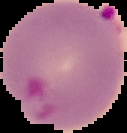

Image is 127×133 pixels. Segmented cell region on a black background. From a thin blood smear. Malaria status: parasitized.